Report the malaria status of this cell.
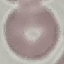
It is uninfected.

Giemsa-stained preparation. Thin blood smear. Acquired by smartphone through the microscope eyepiece. Cell patch, automatically extracted from a larger field of view and resized to 64 × 64 pixels.